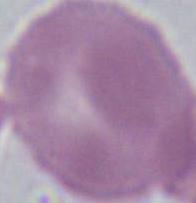
Summary:
  - Modality: photomicrograph
  - Magnification: 1000x
  - Identification: red blood cell